Outline each blood parasite and name the species.
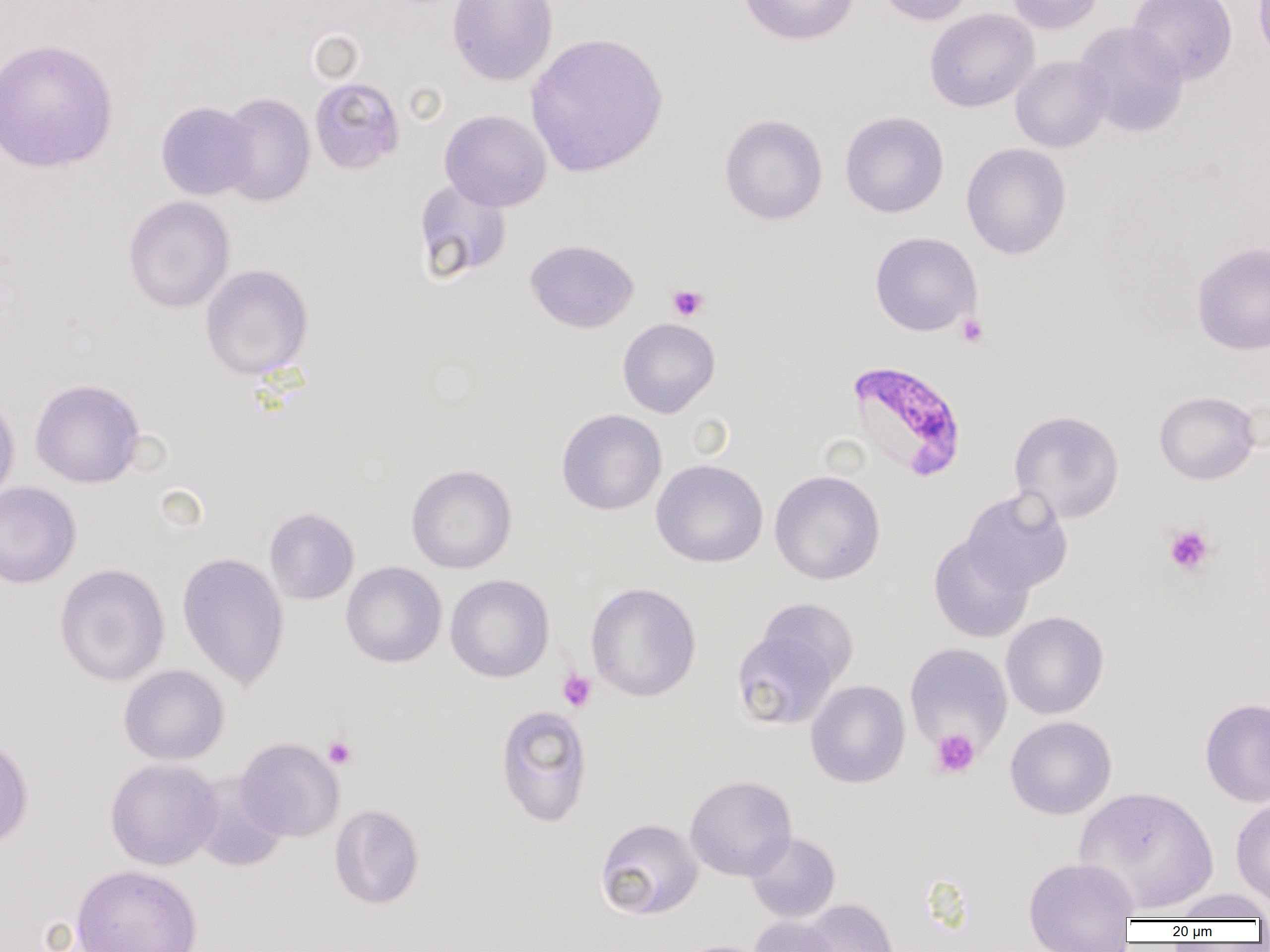

Approximate bounding boxes as [x1, y1, x2, y2] in pixels.
Plasmodium falciparum-infected red blood cells: [846, 362, 967, 482].
No Plasmodium ovale, Plasmodium malariae, Plasmodium vivax, Babesia divergens, or Trypanosoma brucei observed.

slide-level diagnosis = Plasmodium falciparum
modality = light microscopy
magnification = 1000x
platelet locations = approximate bounding boxes as [x1, y1, x2, y2] in pixels: [668, 284, 708, 321], [956, 313, 989, 348], [1164, 524, 1215, 576], [557, 668, 597, 712], [931, 728, 980, 778], [323, 736, 356, 769]
image size = 1270×952 pixels
preparation = thin blood smear
field of view = one of a larger specimen
uninfected red blood cell locations = approximate bounding boxes as [x1, y1, x2, y2] in pixels: [447, 0, 559, 86], [738, 0, 859, 46], [874, 0, 976, 26], [1006, 0, 1105, 34], [1127, 0, 1238, 84], [1253, 0, 1270, 65], [925, 8, 1039, 112], [1074, 22, 1189, 137], [525, 32, 668, 178], [0, 38, 118, 173], [1010, 55, 1112, 153], [309, 77, 405, 175], [217, 92, 315, 207], [156, 101, 258, 200], [439, 110, 552, 211], [840, 111, 949, 218], [719, 114, 828, 226], [961, 143, 1071, 259], [414, 179, 512, 283], [123, 196, 235, 313], [869, 232, 982, 337], [525, 239, 639, 333], [1192, 242, 1270, 355], [200, 264, 313, 379], [617, 318, 720, 418], [30, 378, 146, 488], [1154, 391, 1259, 485], [0, 395, 20, 507], [557, 409, 666, 515], [1009, 410, 1124, 522], [651, 459, 768, 568], [406, 464, 517, 574], [770, 469, 885, 585], [0, 481, 81, 588], [962, 487, 1073, 594], [265, 507, 359, 604], [929, 535, 1034, 643], [177, 551, 290, 690], [54, 562, 170, 686], [341, 562, 446, 668], [446, 574, 554, 682], [586, 583, 701, 701], [756, 598, 858, 688], [1001, 611, 1109, 719], [732, 629, 839, 730], [905, 642, 1012, 754], [118, 665, 229, 765], [806, 680, 910, 788], [1200, 697, 1270, 807], [496, 704, 592, 827], [1005, 716, 1116, 819], [0, 733, 34, 850], [235, 737, 344, 842], [104, 758, 223, 870], [189, 773, 288, 872], [685, 775, 797, 881], [1074, 786, 1219, 915], [1231, 797, 1270, 909], [329, 804, 425, 910], [595, 818, 703, 920], [746, 832, 840, 923], [1023, 856, 1140, 950], [71, 864, 203, 952], [1169, 888, 1269, 922], [802, 899, 899, 952], [749, 916, 841, 952], [673, 939, 776, 952]